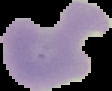

malaria_status: parasitized
image_size: 112×91 pixels
image_type: segmented cell region with the area outside set to black
preparation: thin blood smear